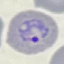

Result: malaria parasites identified. Automatically extracted cell patch, resized to 64 × 64 pixels. Thin smear of blood. Giemsa-stained preparation. Photographed with a smartphone camera at the microscope eyepiece.